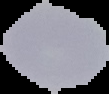

Summary:
  - Image type: segmented cell region on a black background
  - Preparation: thin blood smear
  - Image size: 109×94 pixels
  - Result: no Plasmodium parasites seen